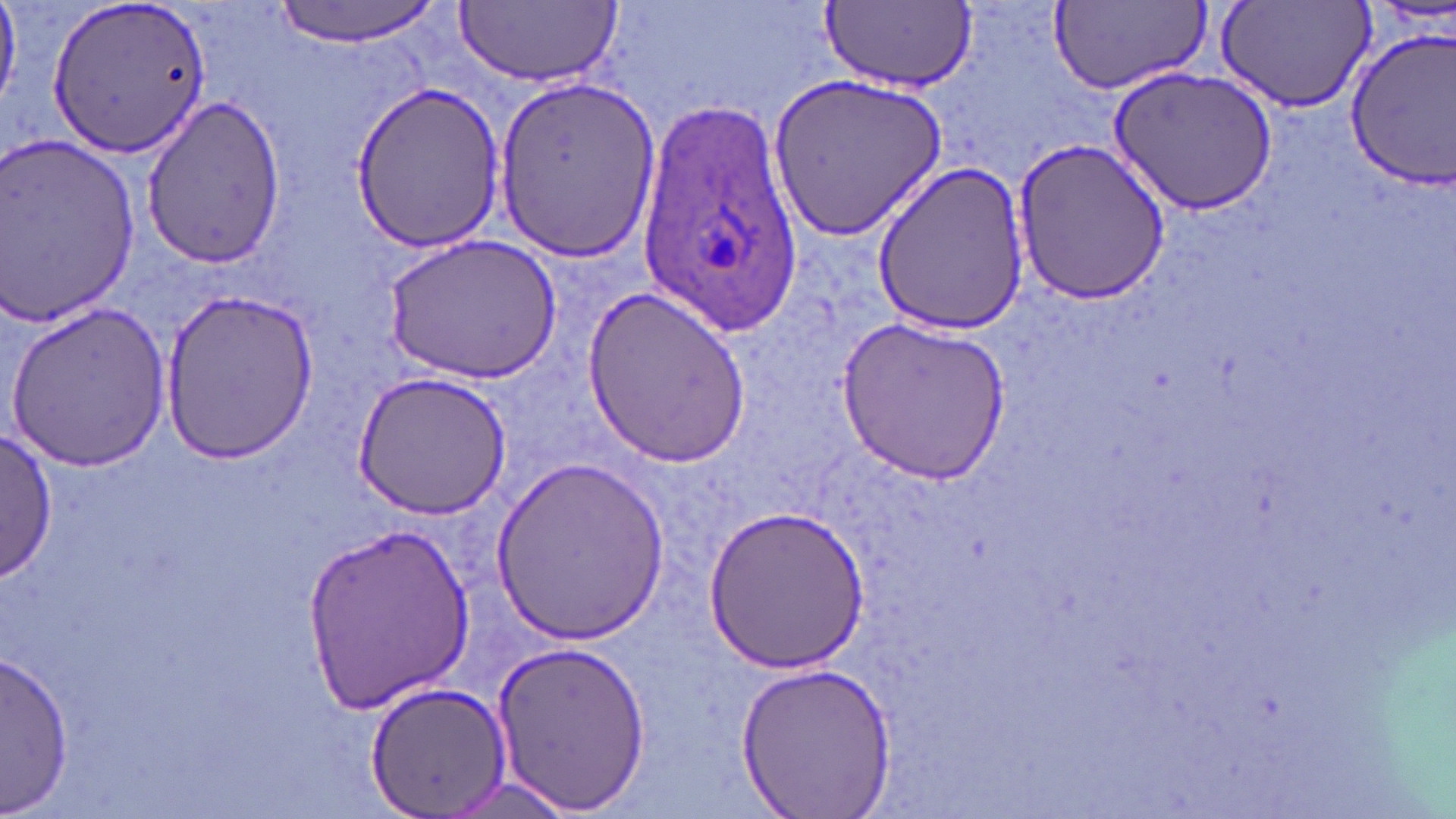
Approximate bounding boxes as named x1/y1/x2/y2 corners in pixels. Uninfected red blood cell locations: (x1=271, y1=0, x2=445, y2=45), (x1=455, y1=0, x2=621, y2=86), (x1=1048, y1=0, x2=1209, y2=98), (x1=46, y1=1, x2=214, y2=159), (x1=820, y1=1, x2=977, y2=91), (x1=1214, y1=3, x2=1375, y2=115), (x1=1342, y1=26, x2=1456, y2=189), (x1=1107, y1=66, x2=1278, y2=216), (x1=771, y1=70, x2=948, y2=238), (x1=490, y1=75, x2=661, y2=264), (x1=348, y1=81, x2=506, y2=251), (x1=138, y1=94, x2=286, y2=270), (x1=0, y1=135, x2=145, y2=329), (x1=1009, y1=135, x2=1171, y2=306), (x1=871, y1=160, x2=1031, y2=335), (x1=385, y1=234, x2=560, y2=384), (x1=581, y1=283, x2=750, y2=468), (x1=158, y1=288, x2=319, y2=464), (x1=7, y1=301, x2=170, y2=469), (x1=839, y1=315, x2=1013, y2=485), (x1=350, y1=371, x2=512, y2=519), (x1=1, y1=431, x2=57, y2=582), (x1=490, y1=453, x2=671, y2=645), (x1=705, y1=503, x2=871, y2=674), (x1=301, y1=521, x2=476, y2=711), (x1=489, y1=637, x2=653, y2=815), (x1=0, y1=650, x2=75, y2=813), (x1=735, y1=661, x2=895, y2=818), (x1=362, y1=677, x2=514, y2=819), (x1=436, y1=773, x2=582, y2=817). Plasmodium ovale-infected red blood cell locations: (x1=635, y1=101, x2=807, y2=335). Slide-level diagnosis: Plasmodium ovale. May-Grünwald-Giemsa stain. One field of a larger specimen. Optical microscopy. Thin blood smear. Image is 1456×819 pixels. 1000x magnification.